Assess this cell for malaria.
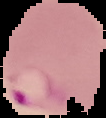
Parasitized.

Summary:
  - Image type: segmented cell region with the area outside set to black
  - Image size: 106×118 pixels
  - Preparation: thin blood film